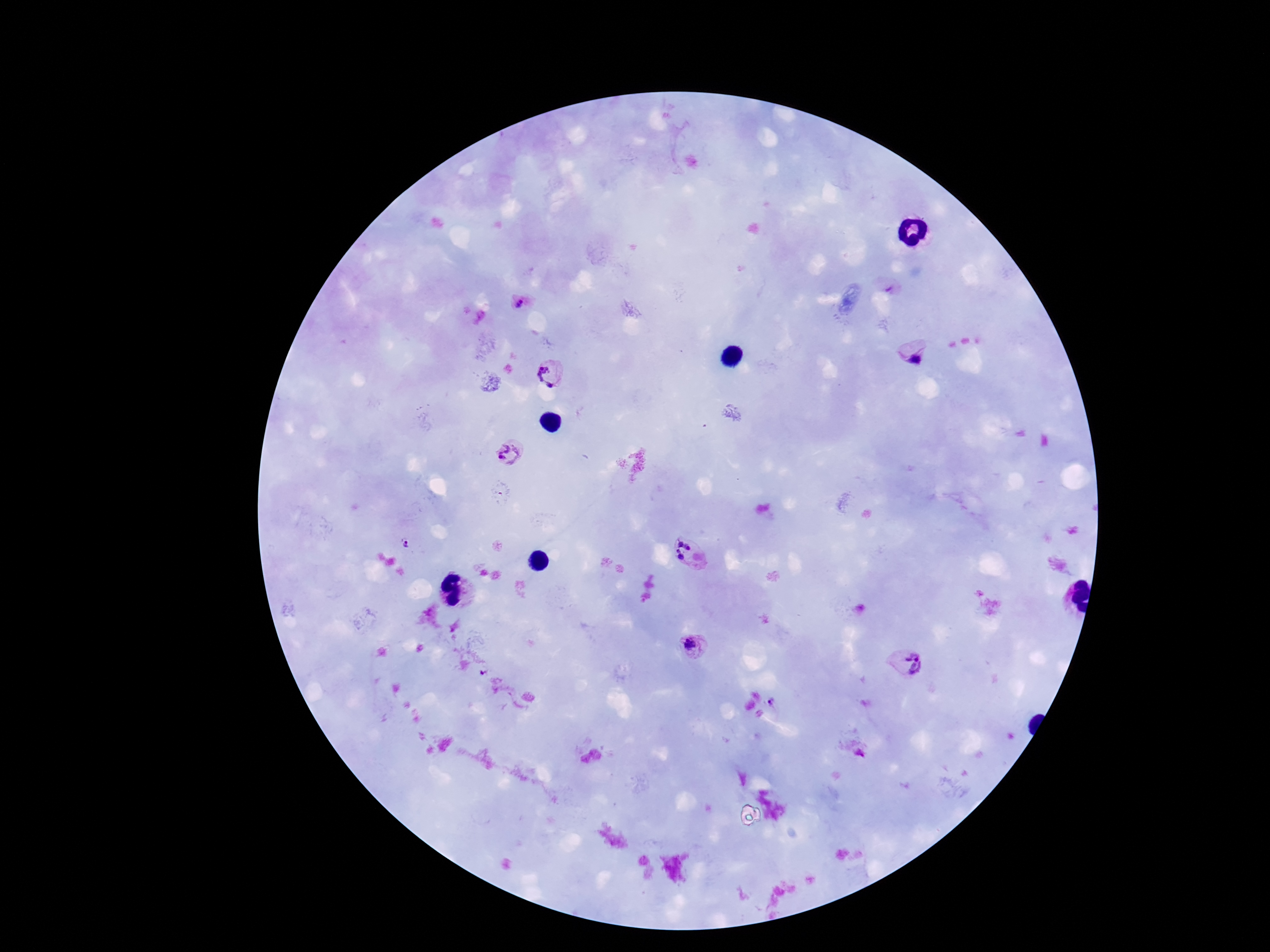
Approximate centers as {x, y} in pixels. Plasmodium parasite locations: {519, 305}, {915, 355}, {550, 373}, {508, 456}, {408, 545}, {690, 553}, {691, 646}, {907, 663}, {773, 702}, {859, 754}. One field from this slide. Image is 1270×952 pixels. Thick blood smear. Photographed through the microscope eyepiece with a smartphone camera. 100x magnification. Giemsa stain. Patient malaria status: positive.